Locate every blood parasite and identify its species.
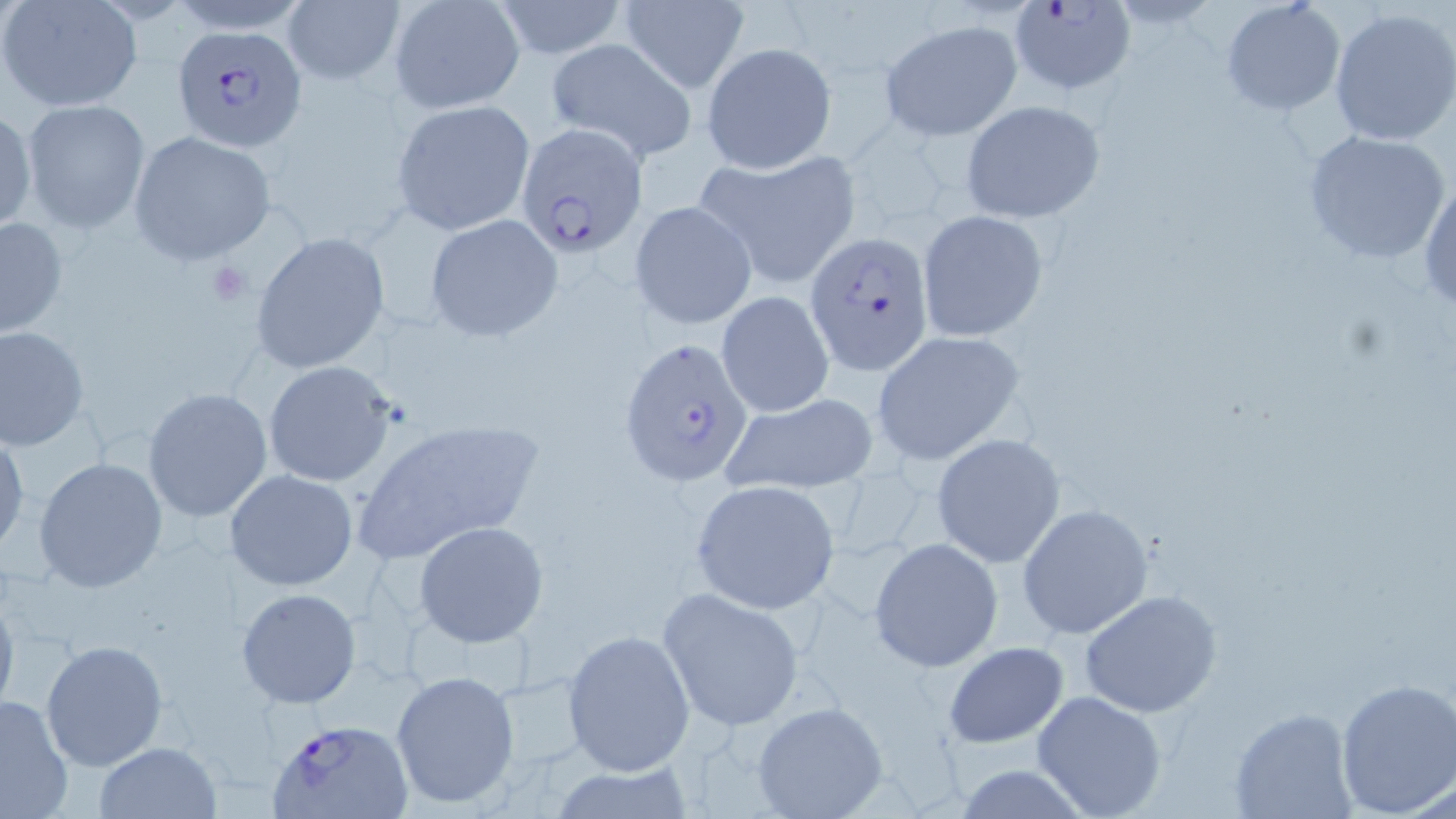
Approximate bounding boxes as (x1, y1, x2, y2) in pixels.
Plasmodium falciparum-infected red blood cells: (1014, 0, 1138, 94), (171, 26, 305, 151), (516, 125, 647, 256), (805, 234, 935, 373), (618, 336, 756, 488), (266, 718, 416, 819).
No Plasmodium ovale, Plasmodium malariae, Plasmodium vivax, Babesia divergens, or Trypanosoma brucei observed.

Summary:
  - Platelet locations: (206, 261, 255, 304)
  - Uninfected red blood cell locations: (1, 0, 143, 113), (491, 0, 630, 59), (1219, 0, 1347, 117), (282, 1, 405, 87), (389, 1, 525, 114), (618, 1, 751, 92), (1329, 7, 1456, 147), (877, 19, 1023, 142), (545, 39, 698, 163), (700, 42, 836, 174), (21, 99, 150, 233), (390, 99, 534, 236), (960, 99, 1107, 224), (0, 105, 35, 236), (1300, 127, 1452, 267), (130, 131, 277, 266), (694, 150, 861, 290), (1419, 175, 1456, 312), (629, 199, 755, 330), (917, 210, 1048, 342), (426, 214, 563, 341), (0, 216, 69, 341), (248, 231, 391, 374), (715, 291, 834, 416), (0, 325, 88, 450), (871, 331, 1027, 468), (263, 360, 398, 488), (141, 386, 273, 523), (717, 392, 880, 496), (353, 416, 544, 563), (0, 430, 28, 557), (931, 431, 1065, 565), (32, 456, 167, 593), (225, 469, 360, 592), (689, 478, 845, 615), (1015, 503, 1153, 641), (414, 521, 549, 647), (869, 537, 1004, 672), (0, 586, 20, 723), (235, 587, 362, 709), (657, 587, 807, 731), (1080, 590, 1224, 717), (561, 629, 696, 775), (40, 638, 168, 772), (942, 642, 1069, 748), (391, 669, 520, 809), (1333, 678, 1456, 816), (1030, 689, 1168, 818), (0, 694, 74, 819), (751, 701, 888, 818), (1230, 708, 1358, 817), (93, 741, 220, 819), (545, 761, 699, 818), (947, 764, 1098, 818)
  - Slide-level diagnosis: Plasmodium falciparum
  - Stain: May-Grünwald-Giemsa
  - Image size: 1456×819 pixels
  - Preparation: thin blood film
  - Field of view: one of a larger specimen
  - Modality: optical microscopy
  - Magnification: 1000x